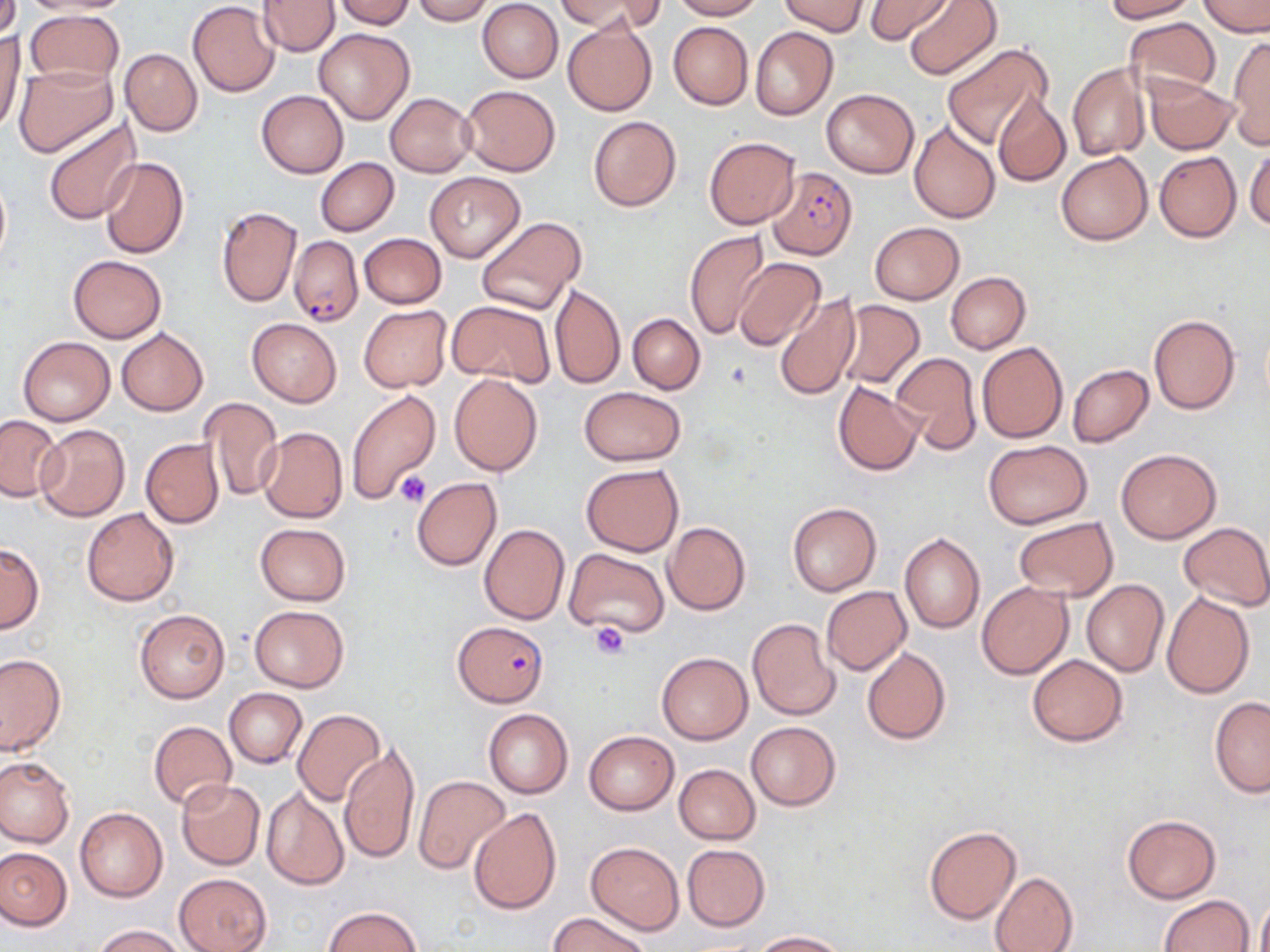

slide_level_diagnosis: Plasmodium falciparum
preparation: thin blood smear
stain: May-Grünwald-Giemsa
field_of_view: one of a larger specimen
image_size: 1270×952 pixels
platelet_locations: 'approximate bounding boxes as (x1, y1, x2, y2) in pixels: (395, 471, 433, 508), (589, 623, 629, 661)'
plasmodium_falciparum_infected_red_blood_cell_locations: 'approximate bounding boxes as (x1, y1, x2, y2) in pixels: (768, 165, 856, 261), (289, 234, 363, 327), (454, 621, 548, 704)'
uninfected_red_blood_cell_locations: 'approximate bounding boxes as (x1, y1, x2, y2) in pixels: (0, 0, 20, 42), (17, 0, 132, 15), (259, 0, 339, 56), (333, 0, 416, 29), (411, 0, 492, 24), (558, 0, 661, 32), (671, 0, 764, 20), (779, 0, 868, 36), (864, 0, 954, 44), (903, 0, 1002, 81), (1104, 0, 1196, 22), (1198, 0, 1270, 37), (477, 1, 562, 82), (187, 2, 280, 98), (24, 8, 123, 87), (562, 18, 658, 117), (1125, 18, 1222, 101), (668, 21, 753, 109), (0, 26, 24, 135), (750, 26, 839, 121), (313, 28, 416, 124), (1227, 35, 1270, 150), (940, 42, 1052, 149), (119, 49, 203, 136), (1068, 63, 1149, 161), (14, 65, 117, 156), (1144, 75, 1239, 154), (460, 84, 560, 177), (821, 87, 919, 177), (257, 90, 348, 178), (386, 92, 477, 177), (993, 93, 1070, 187), (588, 115, 682, 212), (41, 118, 141, 224), (908, 119, 1001, 224), (704, 136, 799, 229), (1246, 146, 1270, 233), (1056, 150, 1154, 246), (1154, 151, 1241, 242), (99, 156, 189, 259), (315, 157, 398, 236), (424, 172, 525, 262), (217, 205, 301, 306), (475, 215, 587, 315), (869, 222, 965, 304), (685, 229, 770, 341), (358, 233, 446, 309), (67, 255, 165, 342), (733, 257, 825, 350), (946, 272, 1031, 353), (550, 283, 625, 388), (773, 292, 860, 402), (448, 300, 554, 388), (834, 300, 925, 390), (359, 305, 453, 392), (1148, 313, 1240, 415), (628, 314, 704, 394), (247, 318, 341, 407), (116, 328, 208, 416), (19, 336, 114, 424), (977, 342, 1068, 443), (888, 352, 981, 456), (1067, 365, 1153, 447), (448, 373, 543, 477), (833, 381, 923, 476), (579, 387, 686, 465), (346, 389, 441, 504), (201, 397, 282, 501), (0, 414, 64, 501), (34, 423, 130, 522), (257, 427, 348, 523), (140, 437, 224, 528), (983, 439, 1092, 529), (1117, 448, 1222, 543), (581, 464, 684, 556), (411, 477, 501, 571), (787, 501, 881, 597), (81, 508, 179, 606), (1013, 517, 1117, 601), (663, 521, 750, 615), (1178, 522, 1270, 610), (255, 523, 351, 606), (480, 524, 569, 624), (899, 531, 985, 634), (0, 543, 43, 633), (565, 549, 669, 638), (1082, 580, 1170, 677), (977, 582, 1072, 678), (820, 586, 911, 675), (1163, 591, 1255, 699), (250, 605, 348, 692), (134, 609, 229, 703), (746, 618, 841, 720), (862, 647, 951, 744), (656, 652, 752, 745), (1, 653, 66, 756), (1027, 655, 1128, 746), (224, 689, 307, 767), (1209, 697, 1270, 797), (293, 709, 386, 806), (484, 709, 573, 798), (149, 720, 236, 809), (746, 720, 840, 811), (584, 730, 678, 815), (339, 741, 420, 864), (0, 756, 74, 847), (675, 764, 760, 844), (414, 775, 510, 873), (176, 779, 266, 869), (261, 785, 349, 890), (74, 806, 168, 902), (468, 807, 562, 916), (1122, 815, 1220, 903), (924, 825, 1022, 926), (585, 841, 684, 934), (682, 844, 770, 931), (0, 847, 71, 930), (990, 872, 1078, 952), (174, 873, 272, 952), (1256, 892, 1270, 952), (1158, 895, 1254, 952), (325, 905, 423, 952), (549, 911, 650, 952), (91, 924, 186, 952), (752, 930, 848, 951)'
magnification: 1000x
modality: optical microscopy